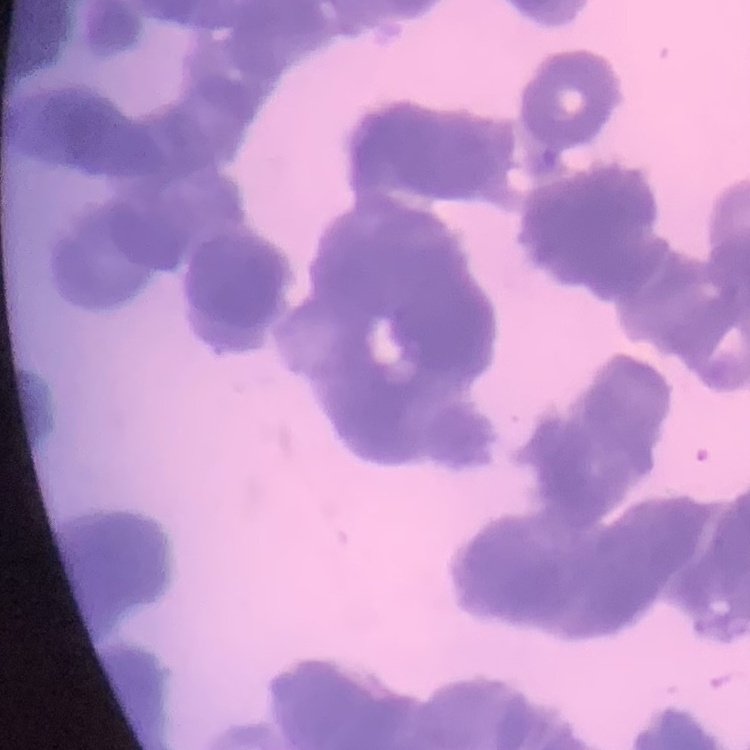

Summary:
  - Red blood cell morphology: rouleaux formation
  - Image type: one tile cut from a larger photomicrograph
  - Preparation: thin blood smear
  - Stain: Field's or Giemsa